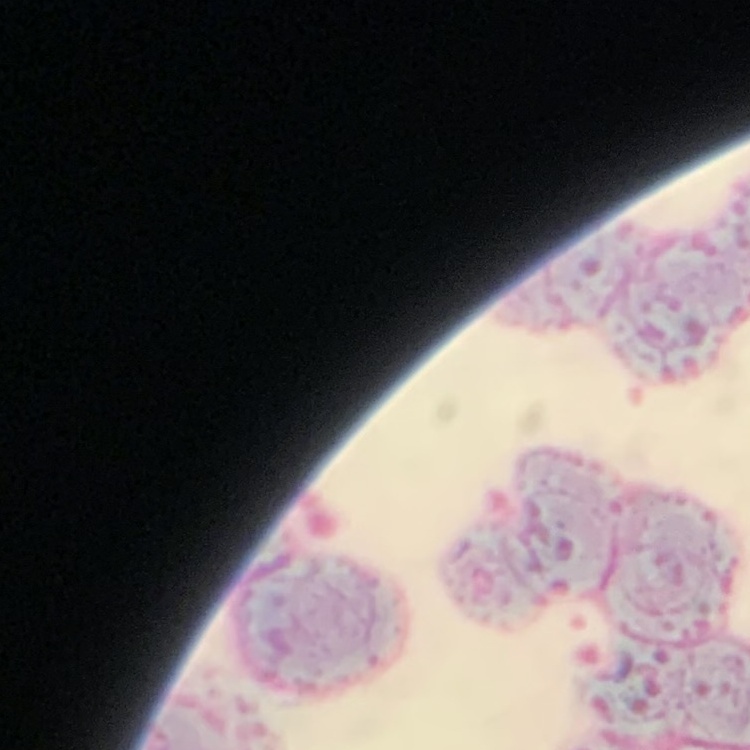

red blood cell morphology = rouleaux formation
image type = one tile cut from a larger photomicrograph
preparation = thin peripheral smear
stain = Field's or Giemsa